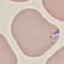

Summary:
  - Result: malaria parasites detected
  - Preparation: thin blood smear
  - Image type: cell patch, automatically extracted from a larger field of view and resized to 64 × 64 pixels
  - Stain: Giemsa
  - Capture: smartphone through the microscope eyepiece